Identify the cell.
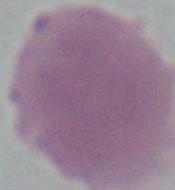
This is an erythrocyte.

{
  "magnification": "1000x",
  "modality": "micrograph"
}